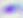 Photomicrograph. Toxoplasma gondii is shown. Captured at 400x magnification.